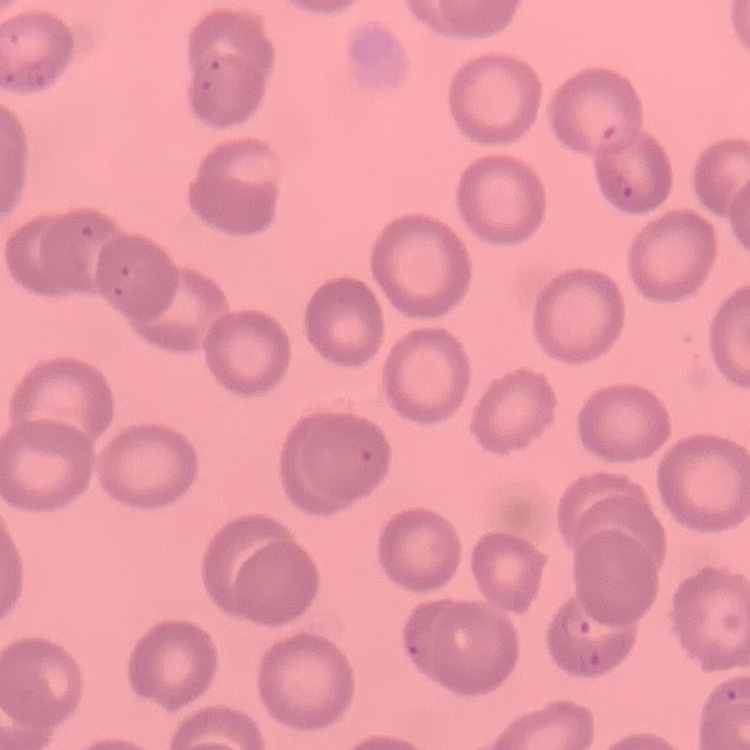

Summary:
  - Red blood cell morphology: no rouleaux formation
  - Preparation: thin peripheral smear
  - Stain: Field's or Giemsa
  - Image type: one tile cut from a larger photomicrograph